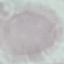 Result: no malaria parasites seen. Photographed with a smartphone camera at the microscope eyepiece. Giemsa-stained preparation. Thin smear of blood. Automatically extracted cell patch, resized to 64 × 64 pixels.